Name the cell type shown.
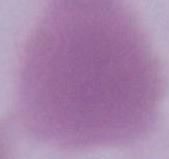

This is an erythrocyte.

Summary:
  - Magnification: 1000x
  - Modality: micrograph